Locate every white blood cell.
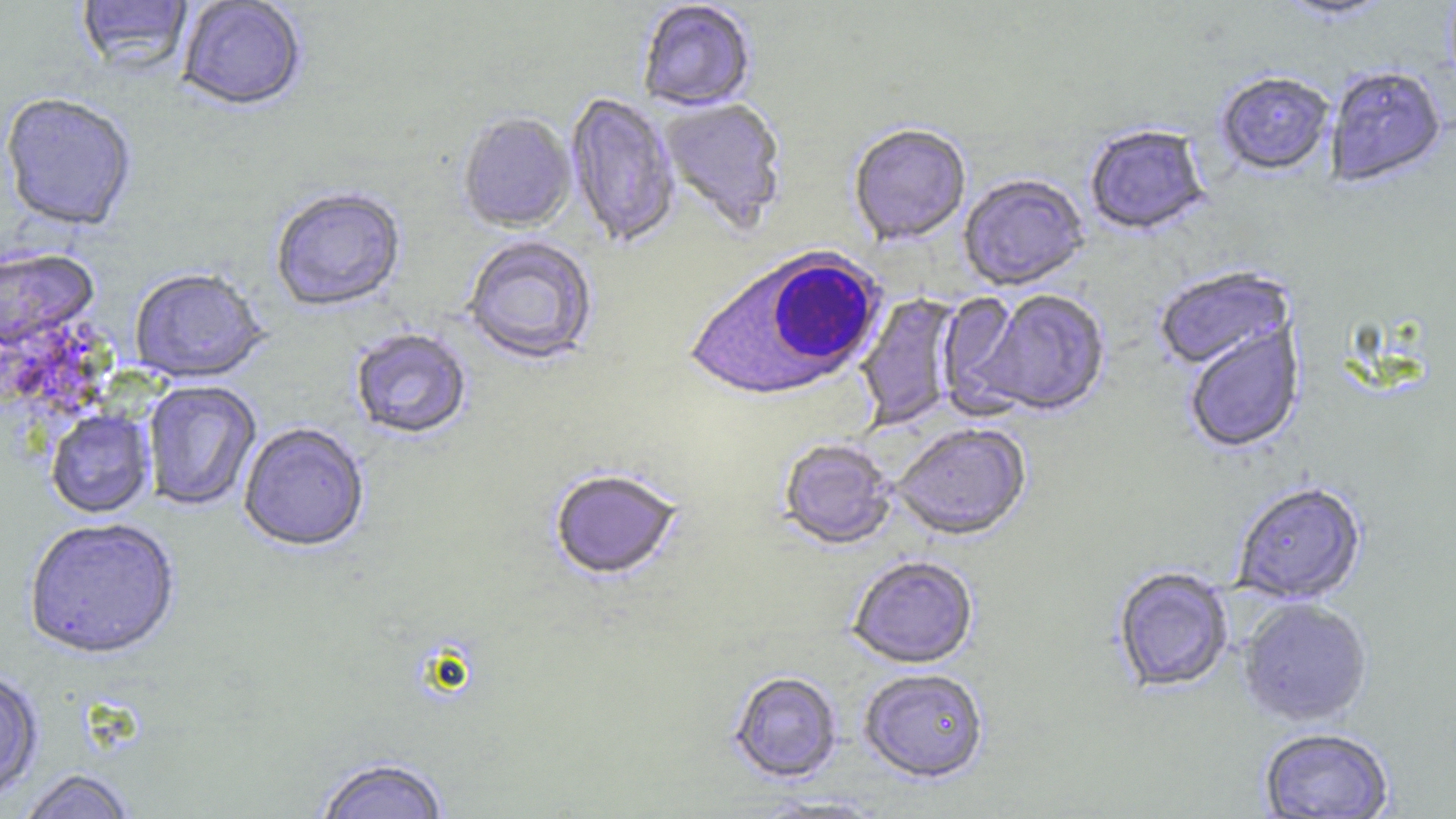
Approximate bounding boxes as named x1/y1/x2/y2 corners in pixels.
White blood cells: (x1=684, y1=248, x2=888, y2=405).

slide-level diagnosis = Plasmodium falciparum
stain = May-Grünwald-Giemsa
uninfected red blood cell locations = approximate bounding boxes as named x1/y1/x2/y2 corners in pixels: (x1=76, y1=0, x2=193, y2=76), (x1=177, y1=0, x2=306, y2=114), (x1=1276, y1=0, x2=1397, y2=23), (x1=637, y1=2, x2=757, y2=114), (x1=1326, y1=68, x2=1446, y2=189), (x1=1216, y1=74, x2=1334, y2=178), (x1=565, y1=92, x2=680, y2=249), (x1=0, y1=95, x2=137, y2=234), (x1=658, y1=98, x2=787, y2=235), (x1=457, y1=114, x2=576, y2=235), (x1=848, y1=126, x2=971, y2=247), (x1=1085, y1=127, x2=1210, y2=238), (x1=958, y1=176, x2=1089, y2=292), (x1=270, y1=189, x2=407, y2=314), (x1=461, y1=238, x2=598, y2=367), (x1=0, y1=247, x2=100, y2=356), (x1=1153, y1=268, x2=1295, y2=374), (x1=129, y1=271, x2=269, y2=386), (x1=972, y1=289, x2=1111, y2=419), (x1=937, y1=290, x2=1033, y2=416), (x1=855, y1=292, x2=964, y2=431), (x1=1185, y1=324, x2=1305, y2=454), (x1=350, y1=329, x2=472, y2=442), (x1=143, y1=381, x2=261, y2=513), (x1=45, y1=409, x2=156, y2=520), (x1=238, y1=424, x2=370, y2=555), (x1=892, y1=425, x2=1031, y2=543), (x1=778, y1=439, x2=897, y2=552), (x1=549, y1=471, x2=683, y2=582), (x1=1232, y1=484, x2=1367, y2=606), (x1=24, y1=520, x2=181, y2=663), (x1=848, y1=557, x2=978, y2=670), (x1=1112, y1=568, x2=1234, y2=693), (x1=1239, y1=599, x2=1373, y2=728), (x1=858, y1=670, x2=989, y2=785), (x1=0, y1=671, x2=44, y2=803), (x1=729, y1=672, x2=842, y2=784), (x1=1258, y1=728, x2=1395, y2=818), (x1=313, y1=758, x2=452, y2=819), (x1=15, y1=770, x2=140, y2=819)
field of view = one of a larger specimen
magnification = 1000x
modality = optical microscopy
preparation = thin blood smear
image size = 1456×819 pixels